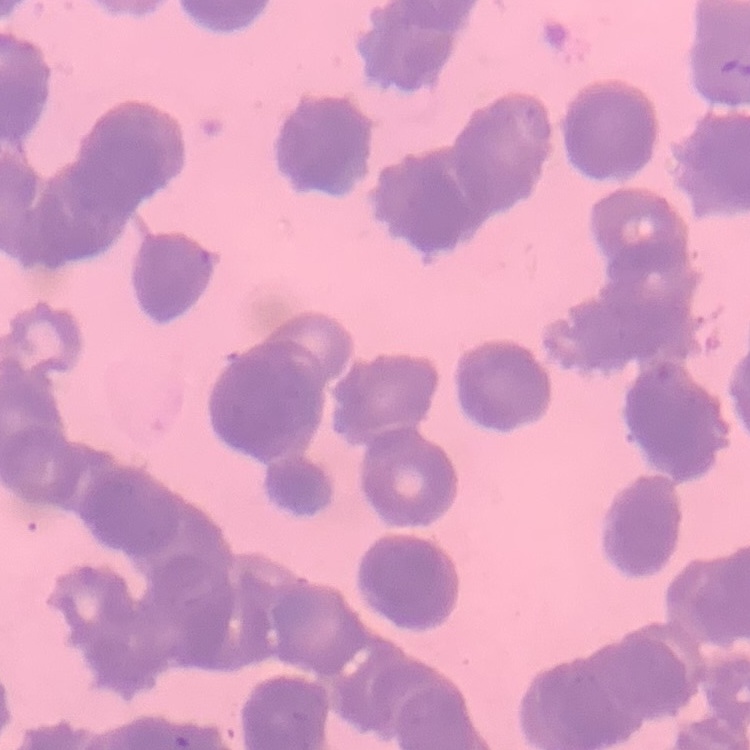

erythrocyte_morphology: rouleaux formation
stain: Field's or Giemsa
image_type: square crop of a larger photomicrograph
preparation: thin peripheral smear